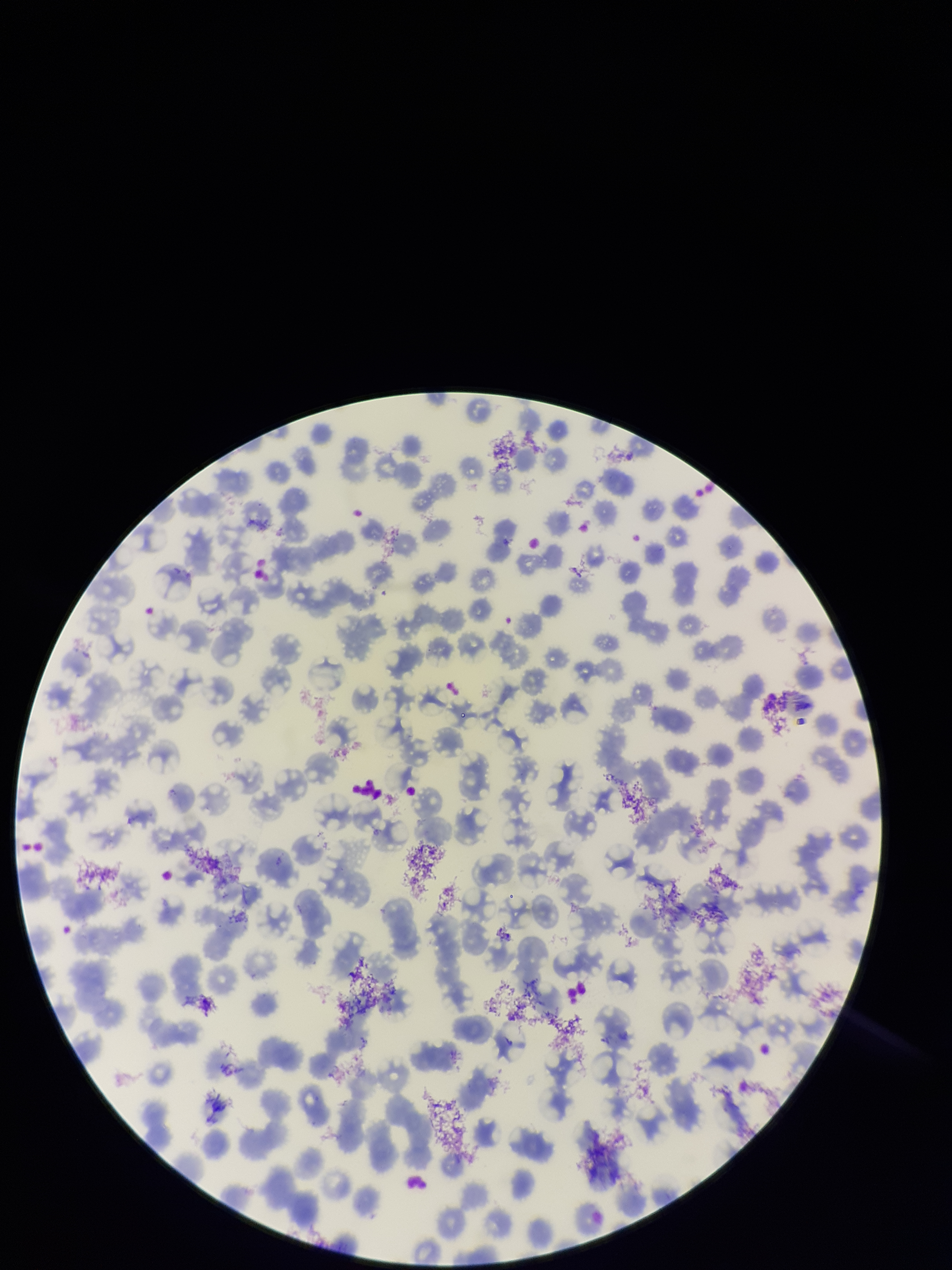
Summary:
  - Patient malaria status: negative
  - Parasitized red blood cells: none detected
  - Parasitized red blood cell count: 0
  - Capture: smartphone photograph through the microscope eyepiece
  - Image size: 952×1270 pixels
  - Red blood cell count: 220
  - Stain: Giemsa
  - Field of view: single
  - Preparation: thin